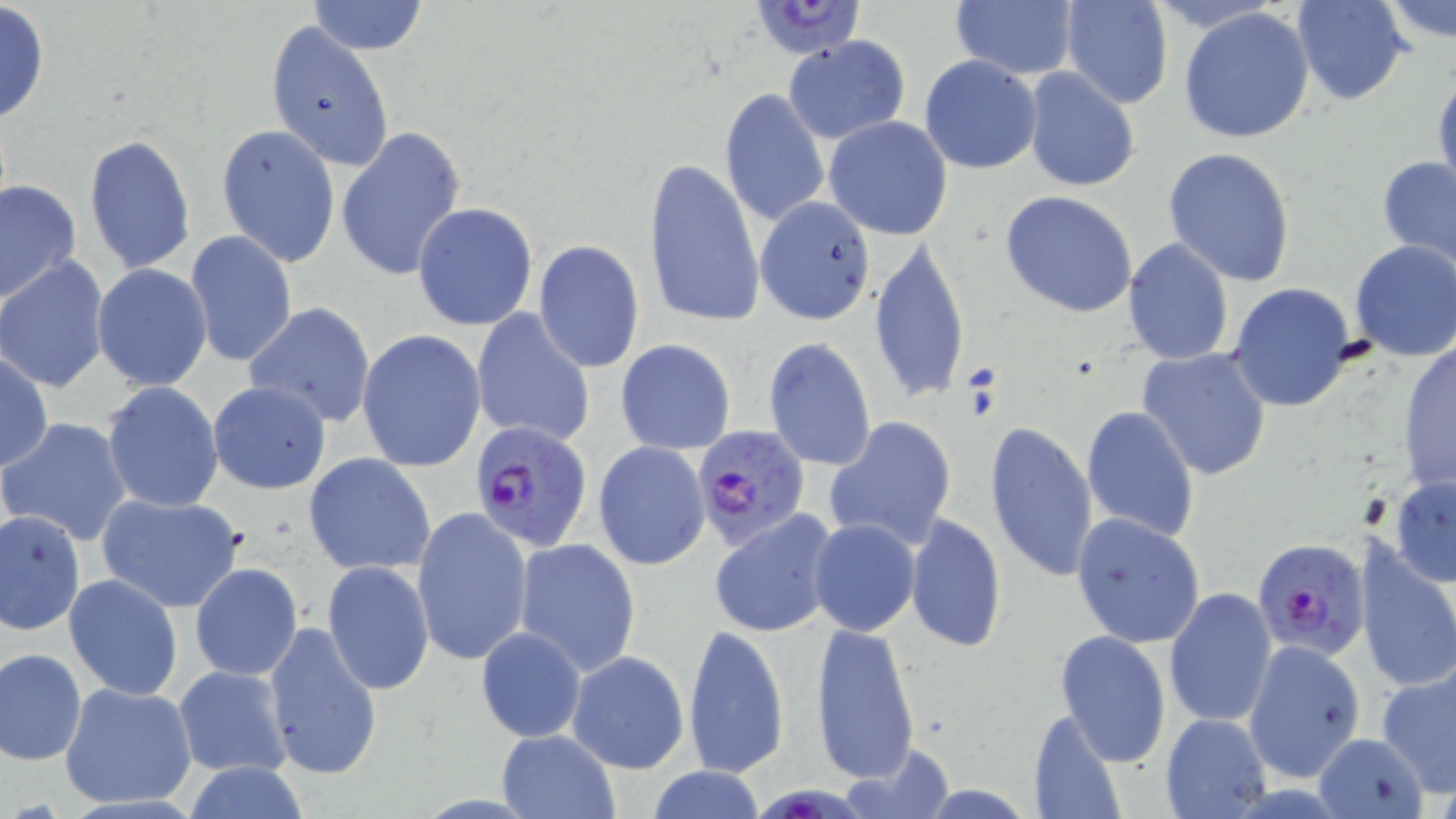
Summary:
  - Coordinate format: approximate bounding boxes as (x1,y1)-(x2,y2) corner pairs in pixels
  - Uninfected red blood cell locations: (305,0)-(428,54), (950,0)-(1081,82), (1291,0)-(1412,106), (1059,1)-(1173,108), (1381,1)-(1456,52), (0,2)-(51,125), (1178,6)-(1315,144), (264,20)-(394,172), (782,35)-(910,144), (919,55)-(1042,175), (1432,63)-(1456,199), (1022,69)-(1140,193), (718,88)-(830,229), (823,116)-(953,240), (215,123)-(340,267), (336,126)-(467,282), (84,132)-(197,275), (1163,146)-(1297,287), (1378,155)-(1456,269), (644,156)-(765,328), (1,180)-(81,305), (1000,191)-(1139,318), (755,197)-(878,323), (412,203)-(539,333), (186,230)-(296,368), (1121,237)-(1235,366), (868,239)-(970,407), (1349,239)-(1456,361), (533,240)-(645,373), (0,259)-(110,393), (92,263)-(214,391), (1228,282)-(1359,413), (245,303)-(376,428), (471,308)-(596,449), (358,330)-(487,473), (763,338)-(877,472), (616,339)-(736,454), (1397,344)-(1456,492), (1136,346)-(1274,482), (0,349)-(52,473), (101,381)-(224,512), (207,381)-(331,495), (1080,405)-(1201,543), (1,416)-(133,546), (825,416)-(957,552), (985,421)-(1098,584), (593,441)-(710,571), (303,452)-(436,576), (1389,474)-(1456,585), (95,490)-(246,612), (411,506)-(532,667), (0,507)-(86,635), (709,511)-(840,637), (1071,512)-(1207,648), (905,513)-(1006,652), (808,518)-(920,637), (512,537)-(642,677), (1353,537)-(1456,695), (322,561)-(434,695), (189,564)-(303,681), (64,574)-(183,699), (1164,587)-(1278,729), (262,620)-(383,780), (810,620)-(920,783), (682,623)-(790,779), (475,626)-(587,743), (1054,630)-(1172,767), (1243,639)-(1366,782), (1,648)-(87,764), (565,650)-(690,775), (1376,661)-(1456,793), (173,665)-(292,778), (60,682)-(197,809), (1028,706)-(1127,819), (1161,712)-(1270,818), (495,729)-(619,819), (1312,732)-(1430,817), (837,745)-(953,818), (178,761)-(314,818), (645,765)-(767,819)
  - Plasmodium falciparum-infected red blood cell locations: (747,2)-(868,61), (469,420)-(595,552), (695,424)-(811,549), (1254,537)-(1370,660)
  - Slide-level diagnosis: Plasmodium falciparum
  - Image size: 1456×819 pixels
  - Field of view: single
  - Modality: optical microscopy
  - Preparation: thin blood film
  - Stain: May-Grünwald-Giemsa
  - Magnification: 1000x